Classify this cell by malaria status.
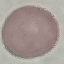
It is uninfected.

capture = smartphone camera at the microscope eyepiece
preparation = thin blood film
image type = automatically extracted cell patch, resized to 64 × 64 pixels
stain = Giemsa